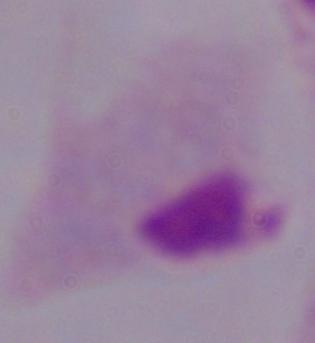
A trichomonad is shown. 1000x magnification. Micrograph.